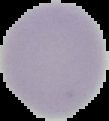
Result: no malaria parasites detected. Cell region segmented out of the field of view; the surrounding area is masked to black. From a thin blood film. Image is 109×121 pixels.